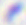

Captured at 400x magnification. Toxoplasma gondii is shown. Micrograph.